Assess for malaria.
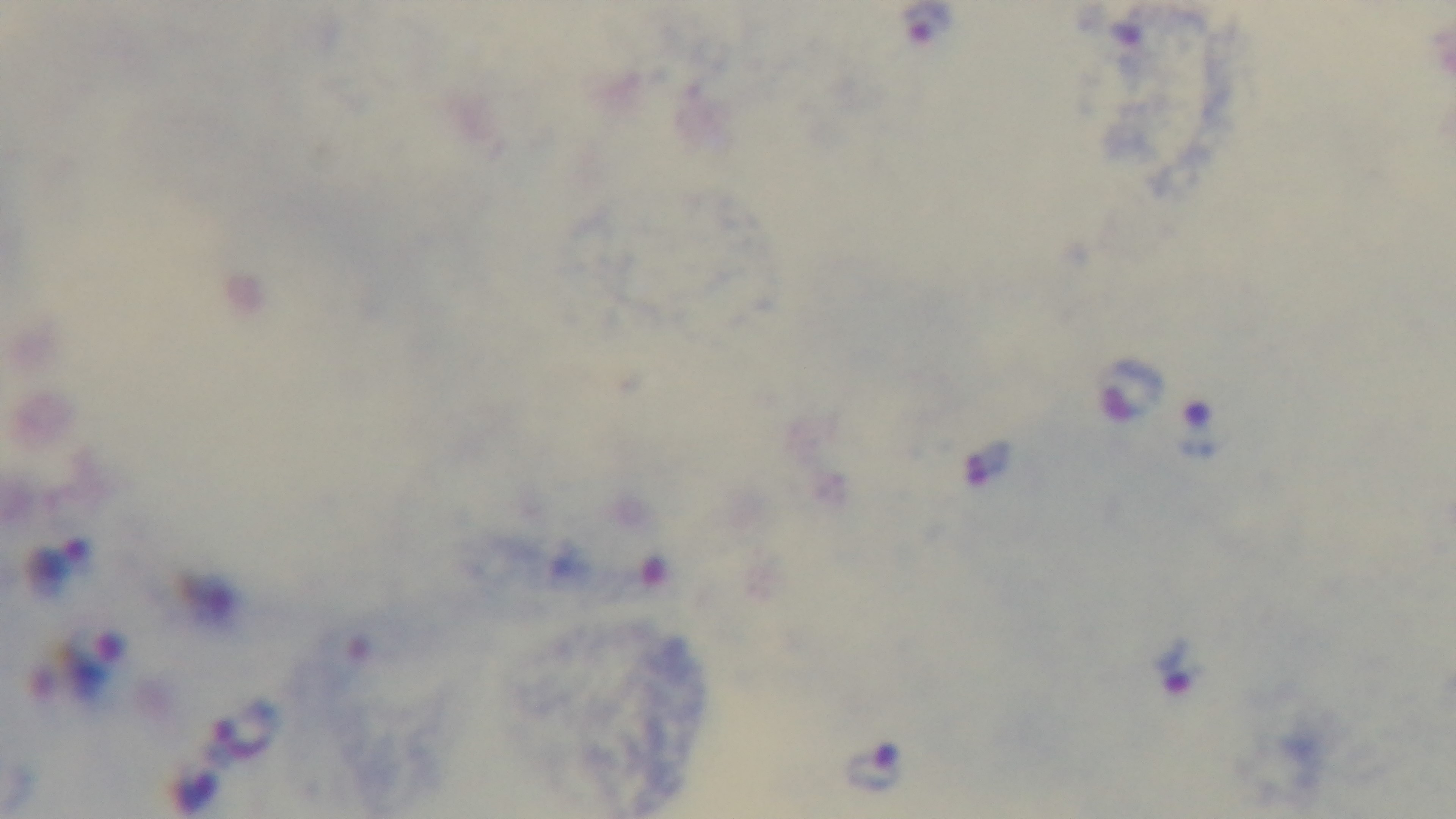
Positive.

100x oil-immersion objective. Photomicrograph. Mounted 4K digital camera. Preparation: thick blood film. Giemsa-stained. Single field of view.